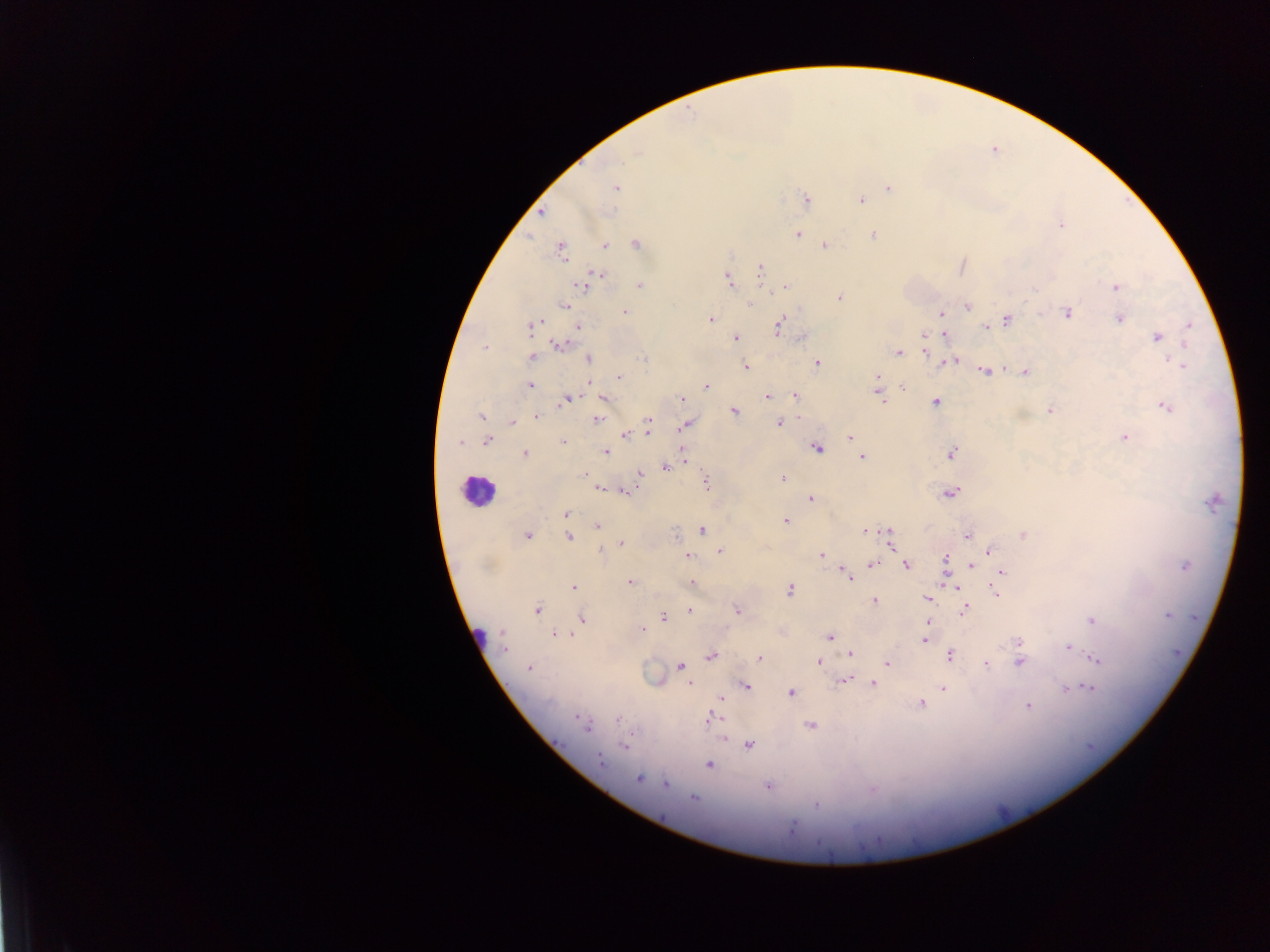
plasmodium_parasite_locations: 'approximate centers as x y in pixels: 636 152; 615 187; 888 188; 805 200; 860 200; 540 213; 1060 224; 795 233; 874 234; 636 244; 824 244; 604 245; 560 249; 961 266; 761 270; 600 274; 728 280; 585 283; 640 285; 784 286; 1115 287; 838 296; 749 303; 565 305; 968 305; 624 311; 1066 312; 940 313; 1119 318; 710 319; 1006 319; 778 326; 1189 326; 531 327; 577 327; 986 328; 944 333; 924 335; 734 337; 1156 337; 804 338; 560 344; 485 347; 926 350; 898 352; 532 356; 589 359; 644 359; 1168 359; 953 360; 947 362; 1175 362; 816 363; 745 366; 1184 366; 1002 368; 984 371; 1025 372; 619 376; 877 376; 530 384; 706 386; 902 387; 879 393; 795 394; 767 396; 604 397; 566 399; 681 399; 935 401; 1166 407; 1051 409; 733 411; 481 416; 536 416; 598 418; 648 421; 511 422; 779 422; 685 425; 648 432; 625 434; 850 437; 1124 437; 486 440; 562 441; 460 442; 816 446; 605 451; 524 453; 951 453; 861 456; 683 459; 665 466; 584 474; 640 474; 782 478; 706 482; 599 488; 623 490; 950 493; 810 498; 1213 501; 566 514; 785 521; 597 526; 702 529; 865 530; 889 534; 1023 534; 526 535; 967 535; 568 537; 890 542; 621 543; 719 550; 988 551; 687 555; 820 555; 947 559; 872 564; 905 565; 971 566; 1185 566; 856 570; 1001 572; 848 576; 630 582; 998 582; 692 583; 954 586; 574 587; 789 589; 995 593; 927 599; 874 600; 537 609; 737 610; 965 610; 689 611; 1167 615; 663 617; 582 618; 1093 620; 641 629; 554 634; 829 637; 925 640; 1018 642; 503 643; 1067 646; 851 652; 950 654; 711 656; 759 658; 1095 660; 818 661; 1020 661; 886 663; 986 663; 680 666; 528 667; 844 679; 689 684; 873 684; 746 685; 1088 687; 942 688; 1065 690; 789 693; 721 698; 920 703; 1028 706; 618 719; 709 719; 582 723; 810 725; 749 744; 625 745; 600 760; 709 764; 638 779; 666 783; 767 786; 693 797; 816 804'
field_of_view: single
country: Ghana
leukocyte_locations: 'approximate centers as x y in pixels: 478 492'
object_labeled_both_plasmodium_parasite_and_leukocyte_by_the_source: 'approximate centers as x y in pixels: 480 637'
image_size: 1270×952 pixels
preparation: thick blood film
capture: mobile-phone photograph through a microscope